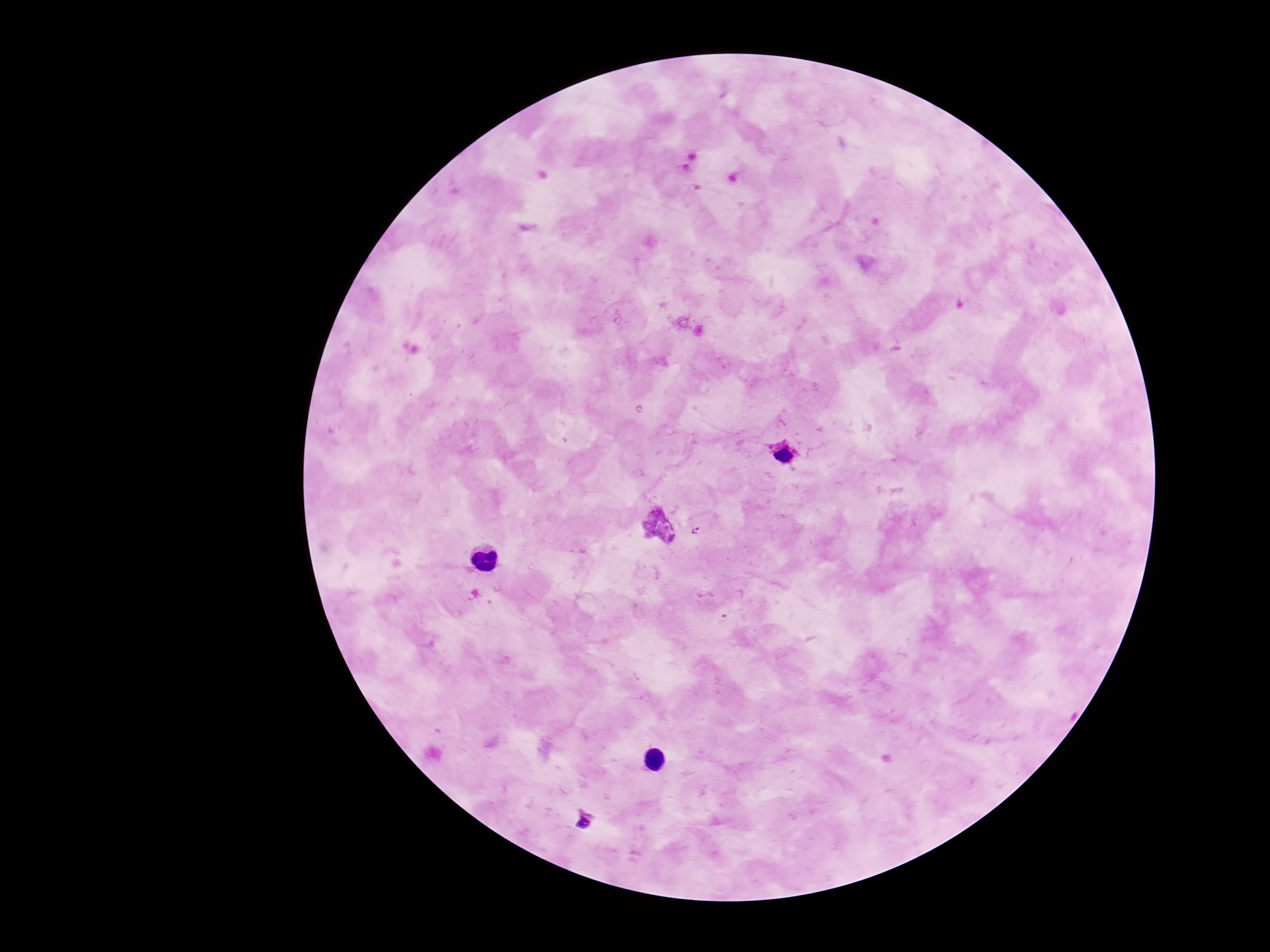

Approximate centers as [x, y] in pixels. Plasmodium parasite locations: [783, 455], [698, 531], [583, 823]. Thick peripheral-blood smear. 100x magnification. Patient malaria status: infected. Photographed through the microscope eyepiece with a smartphone camera. Single field of view. Image is 1270×952 pixels. Giemsa stain.